Give the preparation type.
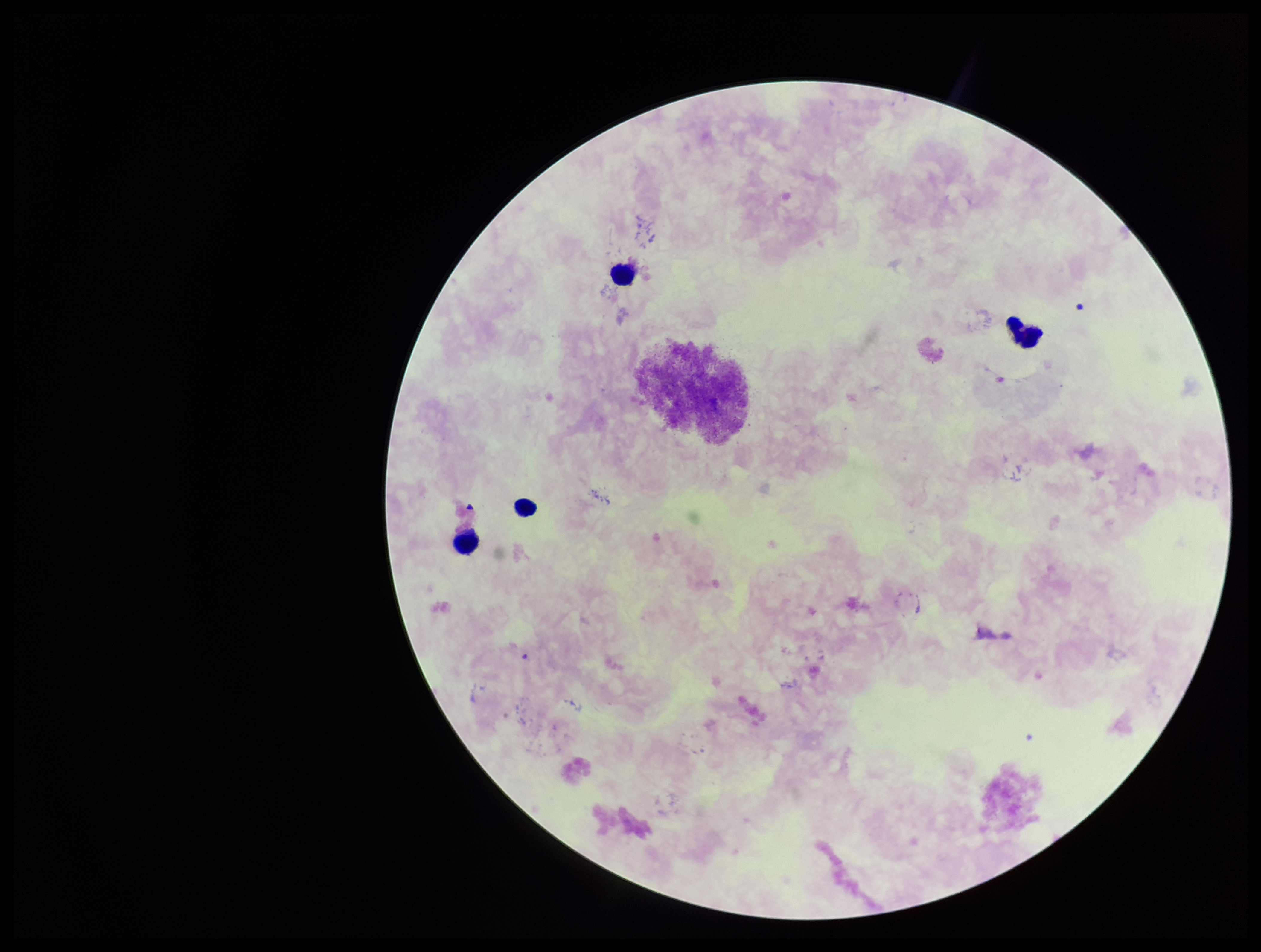

Thick.

parasite_count: 0
stain: Giemsa
leukocyte_count: 4
capture: smartphone photograph through the microscope eyepiece
field_of_view: single
patient_malaria_status: negative
plasmodium_parasites: none identified
image_size: 1261×952 pixels